Report the malaria status of this cell.
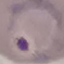

Parasitized.

capture = smartphone camera at the microscope eyepiece
stain = Giemsa
preparation = thin blood film
image type = automatically extracted cell patch, resized to 64 × 64 pixels